Describe the morphology of the red blood cells.
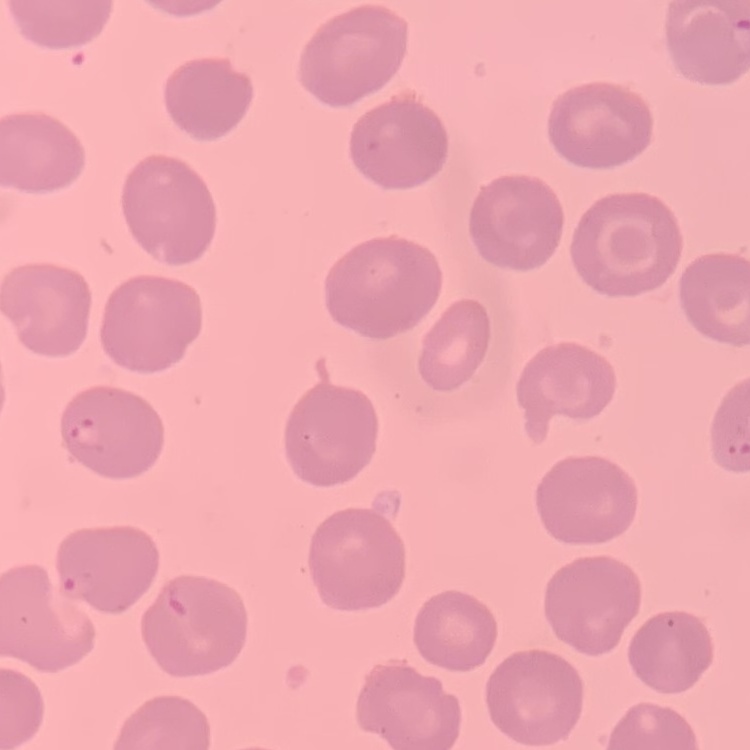

They show no rouleaux formation.

Thin blood smear. Square crop of a larger photomicrograph. Field's or Giemsa stain.